Give the position of every malaria parasite and every leukocyte.
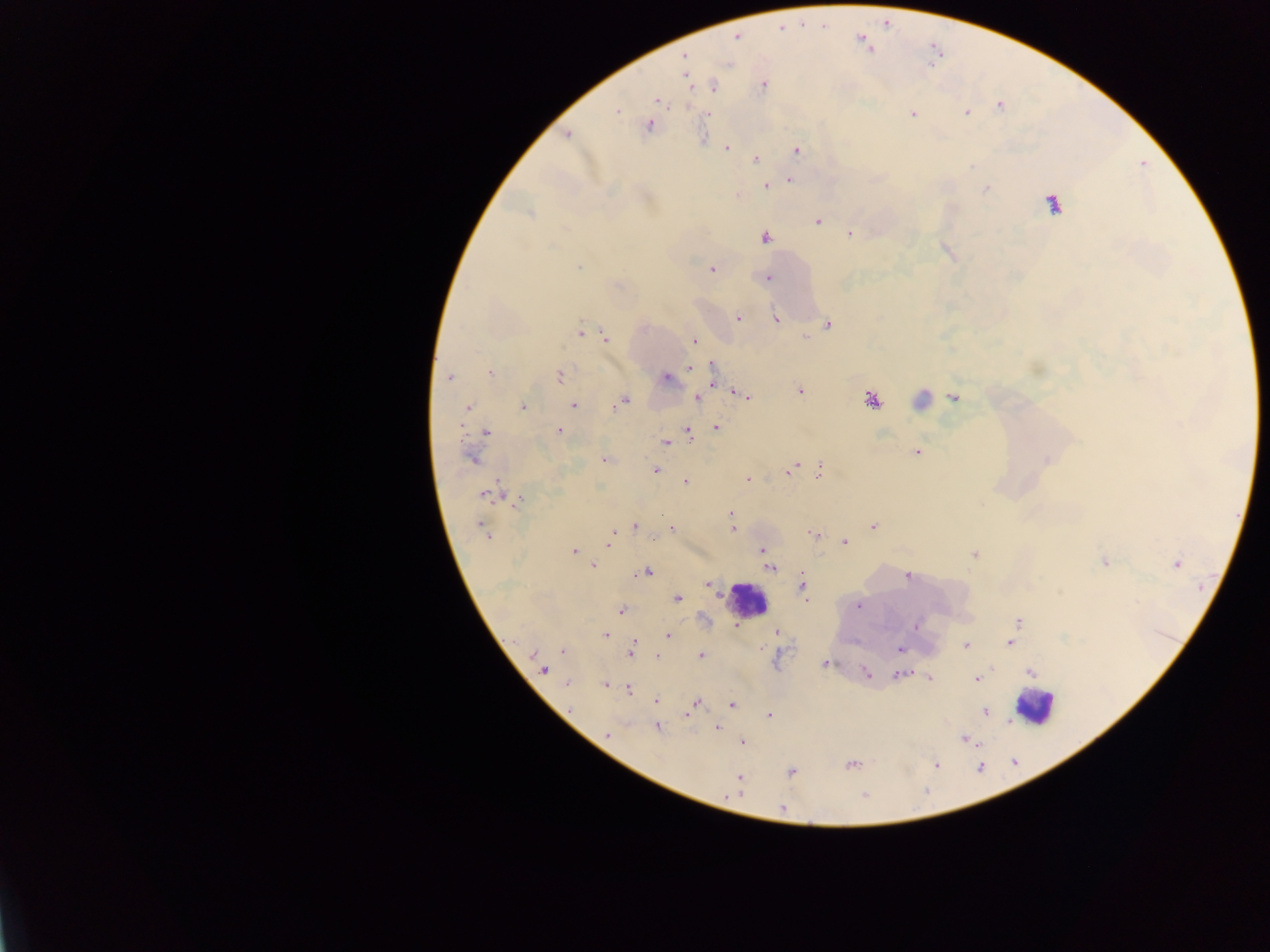
Approximate centers as [x, y] in pixels.
Malaria parasites: [736, 36], [683, 56], [687, 78], [764, 85], [713, 86], [658, 100], [1000, 105], [617, 111], [966, 113], [709, 114], [913, 114], [649, 126], [567, 134], [727, 148], [797, 150], [755, 158], [790, 180], [766, 186], [986, 189], [1052, 205], [529, 214], [817, 222], [850, 234], [765, 237], [578, 268], [712, 269], [767, 278], [738, 317], [776, 319], [828, 325], [581, 333], [605, 338], [693, 340], [712, 366], [689, 369], [490, 373], [560, 375], [449, 378], [666, 378], [800, 391], [744, 396], [698, 398], [954, 398], [871, 399], [621, 401], [573, 406], [468, 407], [524, 407], [716, 427], [688, 430], [559, 431], [487, 432], [673, 439], [665, 442], [917, 452], [471, 459], [1046, 459], [603, 460], [793, 468], [655, 469], [819, 471], [748, 479], [685, 481], [485, 493], [517, 501], [731, 514], [635, 526], [873, 526], [482, 527], [671, 529], [732, 529], [812, 533], [845, 541], [608, 544], [763, 550], [573, 552], [974, 555], [1105, 563], [1176, 564], [593, 566], [771, 568], [646, 572], [907, 576], [708, 585], [802, 585], [677, 598], [859, 605], [621, 611], [1017, 622], [915, 626], [776, 633], [605, 635], [668, 636], [1011, 643], [634, 644], [966, 645], [900, 649], [563, 651], [632, 651], [535, 654], [701, 655], [658, 656], [824, 664], [542, 670], [866, 672], [1030, 672], [900, 675], [930, 678], [977, 679], [567, 683], [605, 684], [629, 690], [656, 700], [695, 703], [732, 705], [985, 711], [688, 713], [769, 715], [657, 728], [717, 728], [607, 734], [965, 740], [743, 742], [852, 765], [936, 765], [791, 772], [739, 778], [864, 796], [782, 809].
Leukocytes: [746, 599], [1034, 707].

Summary:
  - Field of view: single
  - Capture: mobile-phone photograph through a microscope
  - Country: Ghana
  - Preparation: thick blood film
  - Image size: 1270×952 pixels